Report the malaria status of this cell.
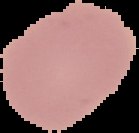
It is uninfected.

From a thin blood film. The area outside the segmented cell region is set to black. Image is 139×133 pixels.